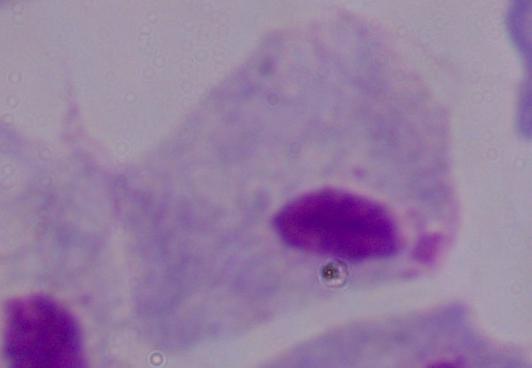

magnification = 1000x
modality = photomicrograph
identification = trichomonad